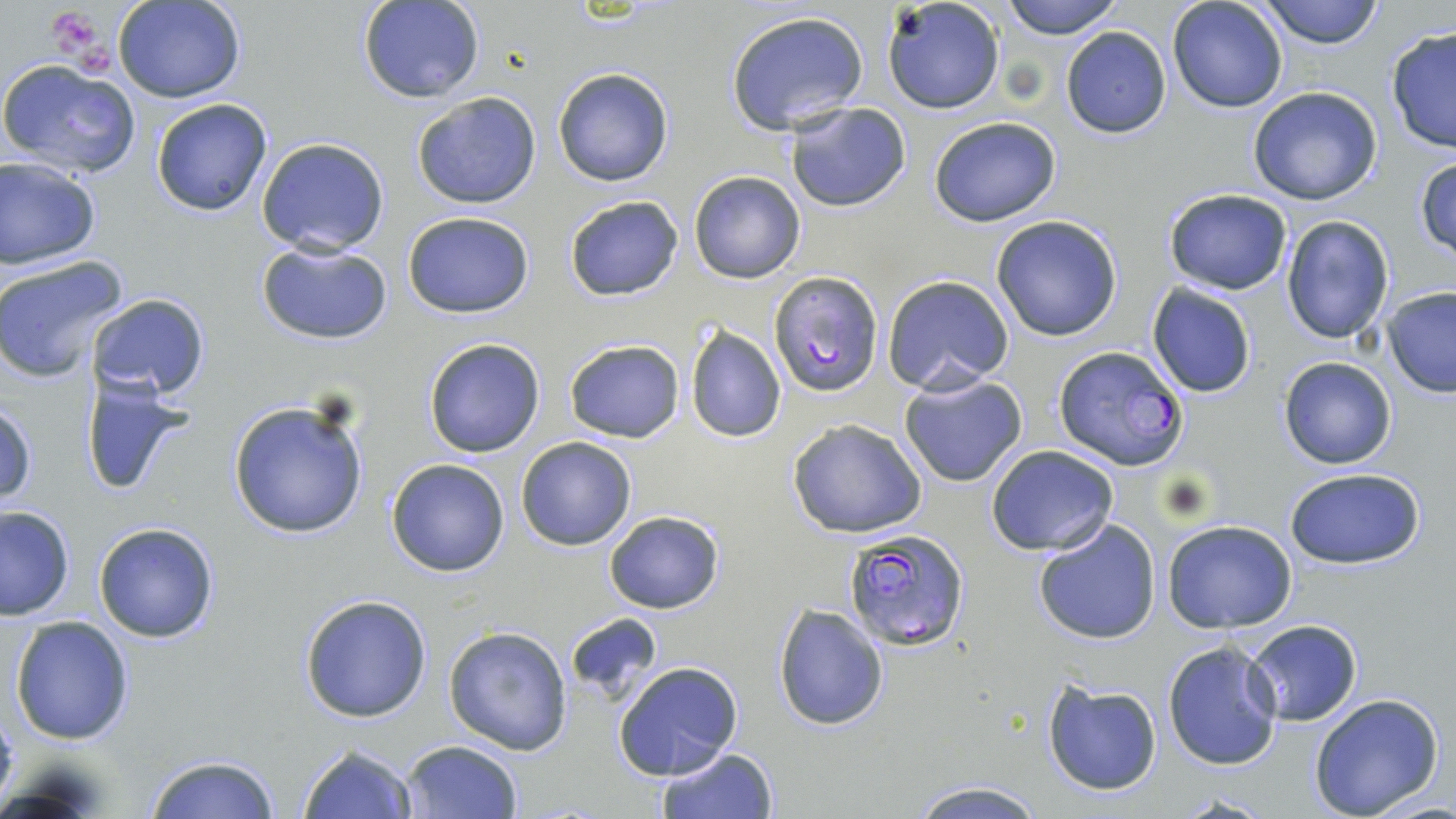
{
  "slide_level_diagnosis": "Plasmodium falciparum",
  "uninfected_red_blood_cell_locations": "approximate bounding boxes as [x1, y1, x2, y2] in pixels: [113, 0, 248, 103], [881, 0, 1004, 116], [999, 0, 1125, 39], [1257, 0, 1384, 49], [357, 1, 485, 103], [1167, 1, 1288, 113], [726, 10, 871, 137], [1384, 25, 1456, 156], [1059, 26, 1171, 139], [0, 57, 142, 178], [552, 66, 676, 188], [1247, 86, 1384, 206], [411, 90, 541, 210], [152, 99, 273, 217], [784, 100, 912, 213], [928, 117, 1062, 226], [257, 137, 390, 257], [1413, 152, 1456, 263], [1, 156, 102, 271], [688, 170, 805, 283], [1163, 188, 1293, 294], [563, 195, 684, 301], [402, 210, 536, 318], [990, 214, 1123, 342], [1280, 215, 1396, 342], [255, 241, 395, 345], [0, 254, 130, 384], [881, 274, 1013, 394], [1145, 281, 1258, 398], [1383, 286, 1456, 396], [84, 292, 212, 402], [684, 323, 786, 443], [423, 337, 545, 458], [564, 339, 685, 444], [1277, 355, 1397, 469], [898, 373, 1028, 487], [77, 374, 193, 500], [227, 399, 371, 540], [0, 400, 37, 508], [786, 418, 928, 538], [515, 436, 638, 552], [984, 444, 1119, 556], [385, 458, 511, 577], [1282, 466, 1428, 568], [0, 505, 75, 621], [603, 508, 725, 614], [1032, 519, 1162, 645], [1162, 520, 1299, 633], [93, 522, 219, 642], [298, 594, 434, 722], [772, 603, 889, 732], [565, 613, 662, 703], [9, 616, 135, 745], [1242, 618, 1363, 727], [443, 625, 574, 755], [1162, 640, 1283, 770], [614, 662, 743, 780], [1041, 679, 1163, 795], [1308, 693, 1445, 819], [400, 739, 523, 819], [297, 742, 420, 818], [655, 746, 780, 818], [143, 753, 282, 818], [906, 778, 1046, 817]",
  "preparation": "thin blood film",
  "modality": "optical microscopy",
  "stain": "May-Grünwald-Giemsa",
  "platelet_locations": "approximate bounding boxes as [x1, y1, x2, y2] in pixels: [48, 6, 110, 64]",
  "magnification": "1000x",
  "plasmodium_falciparum_infected_red_blood_cell_locations": "approximate bounding boxes as [x1, y1, x2, y2] in pixels: [770, 271, 883, 396], [1053, 344, 1189, 469], [840, 527, 970, 650]",
  "field_of_view": "one of a larger specimen",
  "image_size": "1456×819 pixels"
}